Assess this cell for malaria.
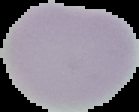
Uninfected.

image_size: 139×112 pixels
image_type: segmented cell region on a black background
preparation: thin blood film